Outline each blood parasite and name the species.
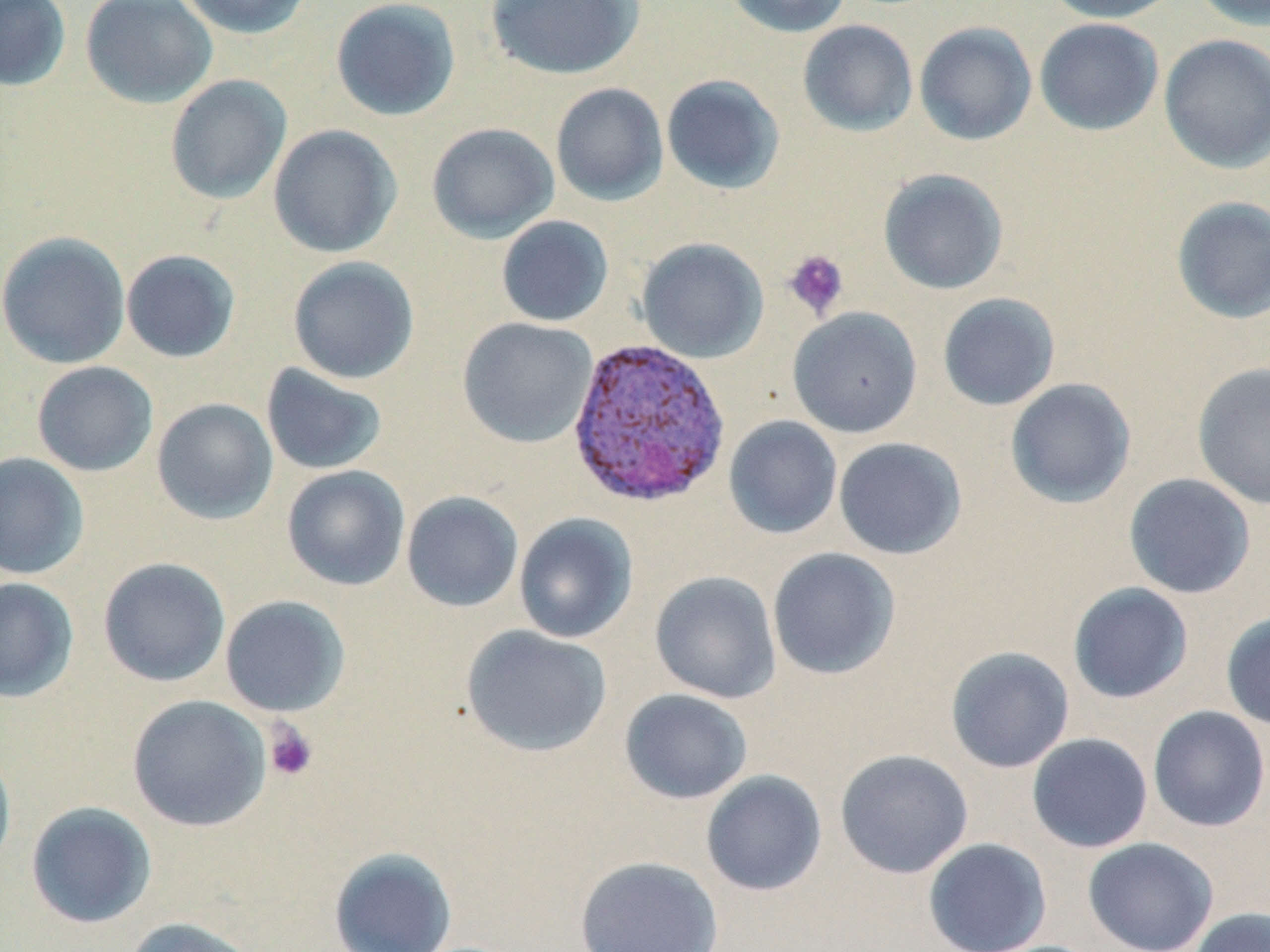
Approximate bounding boxes as (x1,y1)-(x2,y2) corner pairs in pixels.
Plasmodium vivax-infected red blood cells: (566,337)-(731,508).
No Plasmodium falciparum, Plasmodium ovale, Plasmodium malariae, Babesia divergens, or Trypanosoma brucei observed.

Summary:
  - Uninfected red blood cell locations: (0,0)-(71,91), (80,0)-(218,108), (176,0)-(313,39), (330,0)-(462,122), (484,0)-(645,80), (725,0)-(852,38), (1042,0)-(1182,23), (1189,0)-(1270,30), (1034,18)-(1164,136), (797,20)-(918,136), (914,21)-(1037,145), (1158,34)-(1270,173), (164,74)-(292,205), (661,74)-(785,195), (550,83)-(669,206), (426,122)-(559,243), (268,124)-(402,259), (878,168)-(1009,295), (1170,196)-(1270,324), (496,215)-(614,327), (0,231)-(131,369), (636,238)-(769,363), (120,249)-(241,363), (287,256)-(420,385), (937,292)-(1061,411), (787,306)-(922,437), (457,317)-(598,448), (32,361)-(158,477), (1191,362)-(1270,510), (260,363)-(388,476), (1005,378)-(1137,509), (151,398)-(278,525), (724,416)-(842,539), (833,437)-(967,559), (0,452)-(89,580), (281,464)-(411,591), (1123,473)-(1256,599), (401,491)-(524,612), (513,513)-(638,644), (767,547)-(901,680), (97,557)-(231,687), (649,571)-(782,704), (0,577)-(79,703), (1067,582)-(1194,704), (219,595)-(351,717), (1221,611)-(1270,731), (460,625)-(612,758), (945,646)-(1075,773), (619,688)-(753,805), (127,694)-(271,832), (1148,706)-(1270,832), (1026,733)-(1153,853), (0,743)-(16,877), (835,749)-(974,879), (700,770)-(827,896), (25,801)-(157,929), (923,837)-(1052,952), (1082,837)-(1219,952), (328,846)-(458,952), (574,856)-(724,952), (1187,907)-(1270,952), (121,917)-(261,952)
  - Platelet locations: (782,249)-(849,321), (263,719)-(319,782)
  - Slide-level diagnosis: Plasmodium vivax
  - Image size: 1270×952 pixels
  - Preparation: thin blood smear
  - Stain: May-Grünwald-Giemsa
  - Magnification: 1000x
  - Field of view: one of a larger specimen
  - Modality: optical microscopy